Assess this cell for malaria.
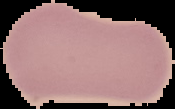

Uninfected.

Summary:
  - Image size: 175×109 pixels
  - Image type: cell region segmented out of the field of view; surrounding area masked to black
  - Preparation: thin blood smear